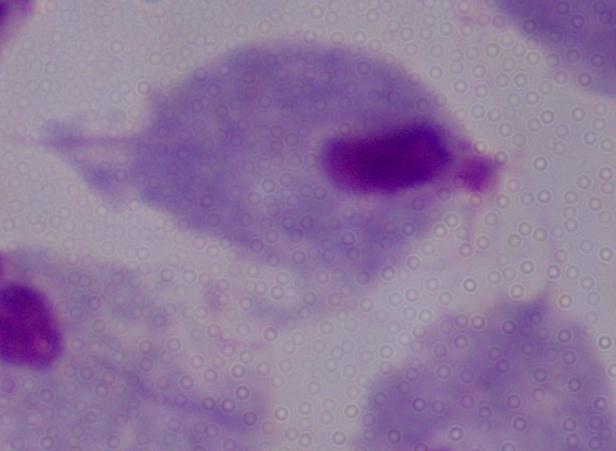
Summary:
  - Modality: micrograph
  - Magnification: 1000x
  - Identification: trichomonad